State which cell type is depicted.
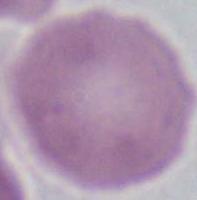

An erythrocyte.

{
  "modality": "photomicrograph",
  "magnification": "1000x"
}